Give the extent of all Plasmodium falciparum-infected red blood cells.
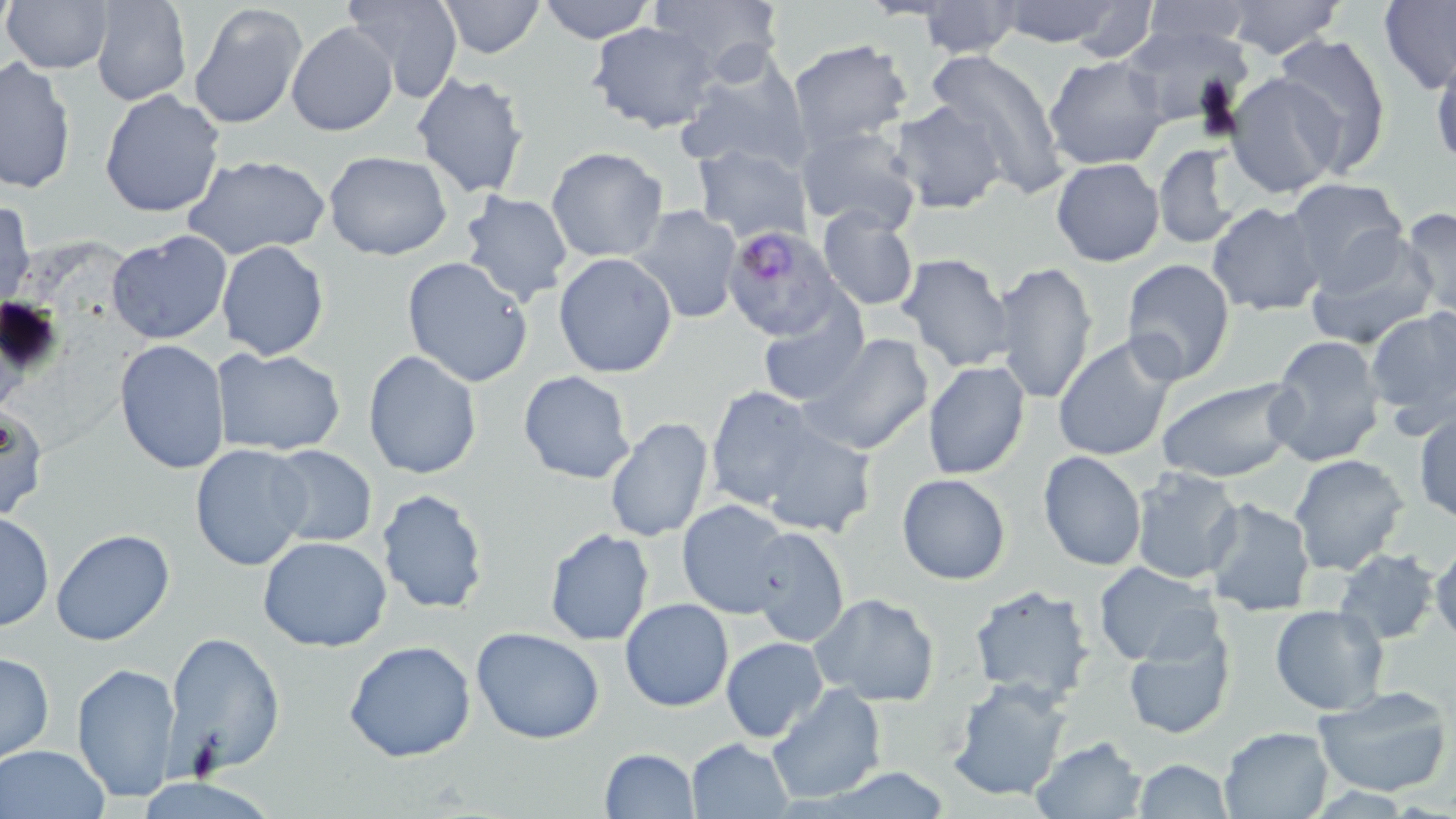

Approximate bounding boxes as [x1, y1, x2, y2] in pixels.
Plasmodium falciparum-infected red blood cells: [723, 222, 845, 343].

Summary:
  - Uninfected red blood cell locations: [2, 0, 114, 74], [89, 0, 193, 107], [342, 0, 463, 102], [435, 0, 546, 57], [537, 0, 656, 43], [649, 0, 789, 77], [917, 1, 1022, 57], [993, 1, 1127, 46], [1224, 1, 1344, 61], [1378, 1, 1456, 96], [1068, 2, 1158, 59], [1134, 2, 1258, 52], [189, 4, 308, 131], [587, 22, 717, 133], [287, 23, 396, 136], [1121, 23, 1254, 130], [1274, 32, 1391, 174], [786, 38, 913, 155], [1429, 45, 1456, 175], [922, 48, 1070, 193], [1044, 56, 1169, 171], [0, 57, 76, 195], [676, 59, 813, 177], [410, 71, 531, 200], [1224, 72, 1345, 198], [98, 90, 225, 218], [890, 99, 1009, 216], [795, 124, 922, 234], [692, 142, 811, 243], [1152, 143, 1244, 249], [547, 146, 669, 262], [323, 151, 454, 260], [181, 153, 332, 261], [1052, 157, 1165, 268], [1284, 178, 1411, 292], [458, 191, 573, 308], [1, 196, 36, 314], [1207, 202, 1326, 316], [627, 204, 744, 326], [816, 205, 921, 312], [1398, 207, 1456, 317], [1304, 229, 1441, 352], [106, 231, 232, 344], [216, 240, 329, 360], [895, 251, 1015, 373], [552, 252, 678, 378], [401, 256, 534, 388], [1120, 259, 1237, 386], [994, 261, 1098, 406], [755, 303, 868, 407], [1364, 306, 1456, 433], [799, 333, 934, 458], [1266, 335, 1388, 469], [1052, 336, 1180, 462], [114, 339, 231, 473], [212, 348, 346, 457], [362, 350, 483, 479], [921, 360, 1031, 480], [518, 370, 637, 484], [1155, 377, 1301, 485], [705, 385, 819, 510], [1, 401, 47, 526], [1413, 409, 1455, 524], [603, 416, 714, 543], [756, 423, 877, 537], [190, 444, 313, 573], [268, 446, 378, 547], [1038, 451, 1147, 571], [1287, 453, 1410, 575], [1130, 466, 1243, 583], [896, 473, 1012, 586], [375, 488, 490, 615], [1201, 497, 1316, 616], [678, 500, 796, 618], [0, 512, 53, 630], [748, 526, 850, 648], [543, 528, 654, 645], [50, 529, 176, 647], [258, 535, 392, 652], [1429, 538, 1456, 646], [1333, 549, 1440, 644], [1093, 562, 1221, 665], [968, 586, 1093, 706], [811, 593, 939, 706], [620, 598, 734, 712], [1270, 604, 1389, 715], [1121, 623, 1236, 741], [471, 628, 605, 746], [163, 632, 285, 775], [720, 636, 826, 740], [343, 639, 477, 763], [0, 652, 53, 761], [72, 661, 182, 804], [948, 676, 1073, 802], [767, 684, 886, 804], [1311, 687, 1456, 798], [1218, 725, 1335, 817], [1030, 736, 1147, 819], [685, 738, 794, 818], [0, 745, 111, 819], [599, 748, 699, 817], [1132, 758, 1235, 819]
  - Slide-level diagnosis: Plasmodium falciparum
  - Stain: May-Grünwald-Giemsa
  - Field of view: single
  - Preparation: thin blood film
  - Magnification: 1000x
  - Image size: 1456×819 pixels
  - Modality: light microscopy